Assess this cell for malaria.
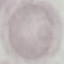
Uninfected.

stain: Giemsa
capture: smartphone through the microscope eyepiece
image_type: cell patch, automatically extracted from a larger field of view and resized to 64 × 64 pixels
preparation: thin blood film